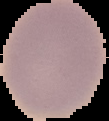
Summary:
  - Preparation: thin blood smear
  - Result: no Plasmodium parasites seen
  - Image type: cell region segmented out of the field of view; surrounding area masked to black
  - Image size: 109×121 pixels